Assess for malaria.
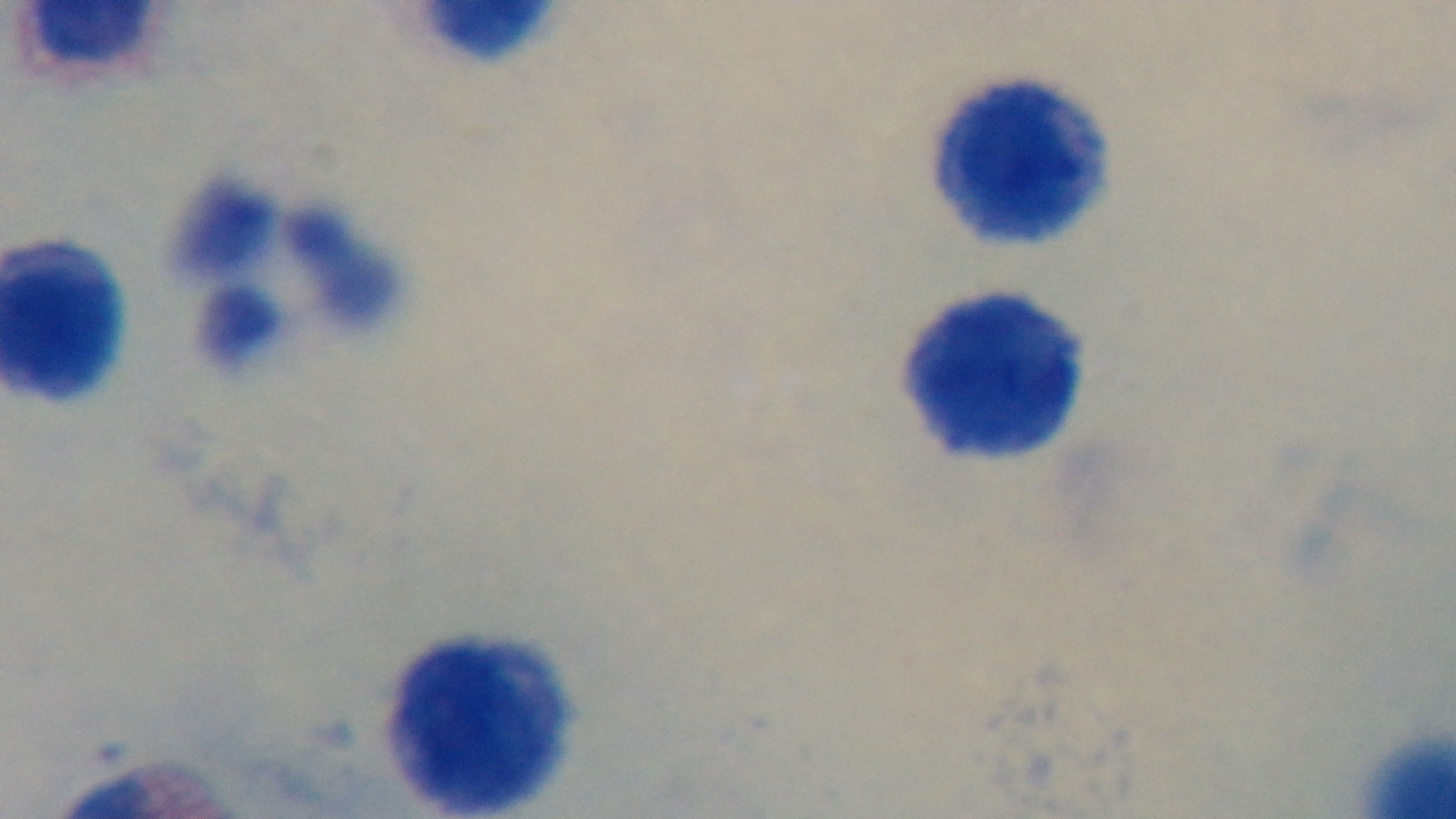

It is uninfected.

Summary:
  - Preparation: thick
  - Objective: 100x oil immersion
  - Capture: mounted 4K digital camera
  - Field of view: single
  - Modality: light microscopy
  - Stain: Giemsa